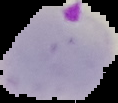 From a thin blood film. Image is 118×103 pixels. Segmented cell region on a black background. Result: malaria parasites detected.